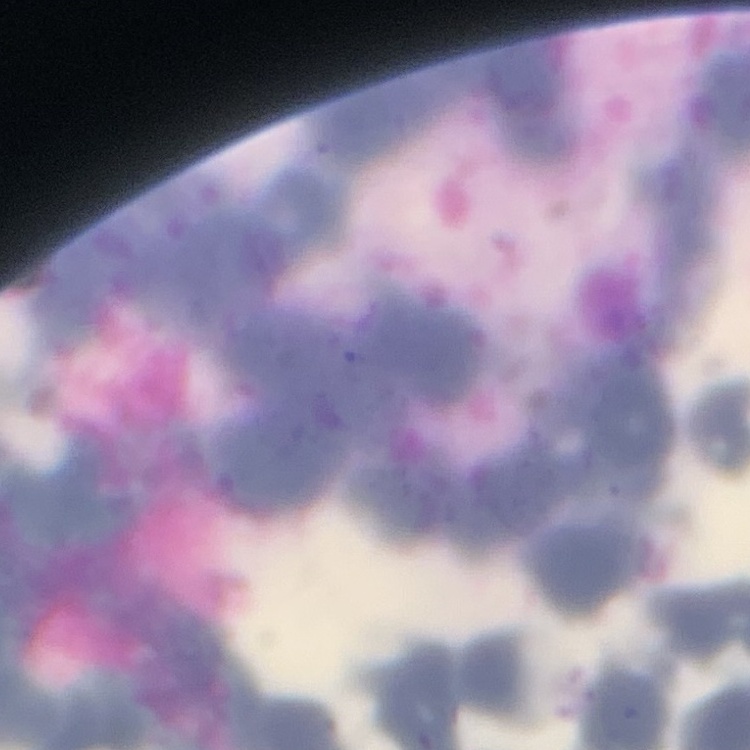
Summary:
  - Erythrocyte morphology: rouleaux formation
  - Image type: square crop of a larger photomicrograph
  - Preparation: thin blood smear
  - Stain: Field's or Giemsa